Classify this cell by malaria status.
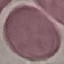
Uninfected.

Summary:
  - Stain: Giemsa
  - Capture: smartphone camera at the microscope eyepiece
  - Preparation: thin blood smear
  - Image type: automatically extracted cell patch, resized to 64 × 64 pixels